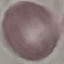

malaria_status: uninfected
image_type: automatically extracted cell patch, resized to 64 × 64 pixels
capture: smartphone through the microscope eyepiece
stain: Giemsa
preparation: thin blood smear